Locate every uninfected red blood cell.
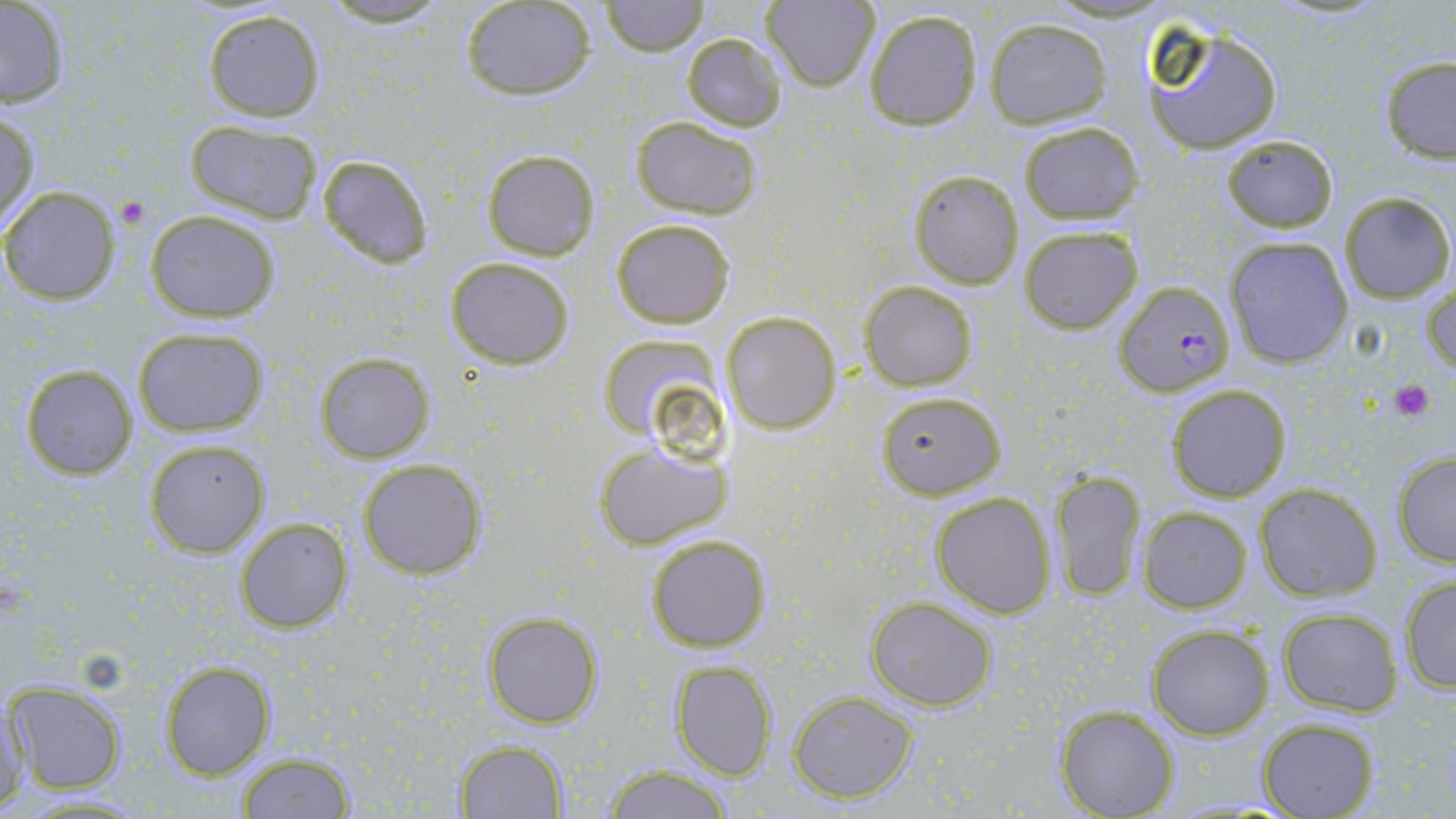

Approximate bounding boxes as (x1,y1)-(x2,y2) corner pairs in pixels.
Uninfected red blood cells: (317,0)-(458,26), (760,0)-(881,90), (602,1)-(707,55), (460,2)-(595,99), (0,3)-(72,109), (200,8)-(326,121), (863,9)-(982,132), (984,18)-(1111,127), (1139,20)-(1286,155), (680,32)-(787,131), (1379,56)-(1456,162), (1,110)-(39,233), (630,116)-(764,220), (182,119)-(324,224), (1016,122)-(1143,225), (1221,134)-(1338,232), (481,149)-(600,260), (315,153)-(433,269), (909,170)-(1024,287), (0,187)-(120,305), (1337,191)-(1453,302), (144,209)-(281,322), (610,217)-(736,330), (1017,224)-(1142,335), (1225,236)-(1354,368), (445,256)-(576,370), (1422,275)-(1455,377), (860,281)-(978,391), (721,312)-(840,434), (132,326)-(267,437), (595,332)-(724,443), (313,352)-(436,463), (17,362)-(140,480), (1164,384)-(1293,502), (875,389)-(1006,499), (144,439)-(270,556), (592,439)-(732,551), (1391,451)-(1456,567), (357,458)-(486,579), (1050,469)-(1146,604), (1254,484)-(1382,601), (929,491)-(1057,618), (1136,505)-(1252,613), (233,517)-(352,634), (645,532)-(773,652), (1399,574)-(1456,692), (865,596)-(997,710), (1275,607)-(1402,716), (482,609)-(603,729), (1146,624)-(1274,738), (157,660)-(276,781), (670,661)-(777,781), (6,682)-(127,795), (788,690)-(919,802), (1,692)-(33,811), (1054,704)-(1181,818), (1255,716)-(1379,819), (455,740)-(569,818), (235,751)-(358,817), (603,765)-(734,819).

Summary:
  - Plasmodium falciparum-infected red blood cell locations: (1113,281)-(1236,397)
  - Platelet locations: (117,198)-(147,228), (1391,379)-(1435,420)
  - Slide-level diagnosis: Plasmodium falciparum
  - Image size: 1456×819 pixels
  - Stain: May-Grünwald-Giemsa
  - Magnification: 1000x
  - Modality: light microscopy
  - Preparation: thin blood smear
  - Field of view: single